Name the blood parasite species.
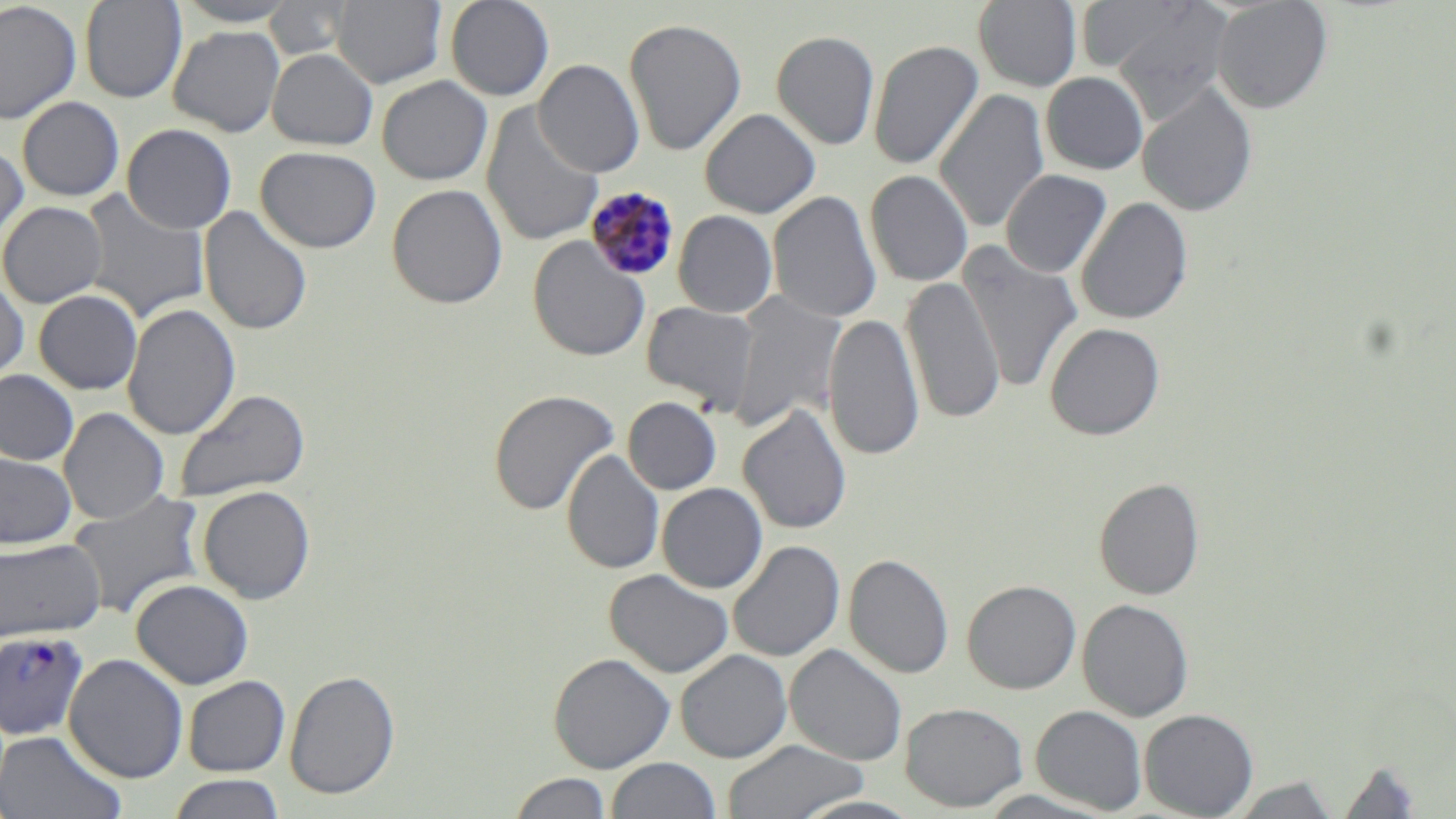

Plasmodium malariae.

Summary:
  - Coordinate format: approximate bounding boxes as named x1/y1/x2/y2 corners in pixels
  - Uninfected red blood cell locations: (x1=79, y1=0, x2=186, y2=102), (x1=172, y1=0, x2=300, y2=27), (x1=266, y1=0, x2=355, y2=62), (x1=332, y1=0, x2=446, y2=87), (x1=445, y1=0, x2=555, y2=101), (x1=1212, y1=0, x2=1332, y2=113), (x1=0, y1=1, x2=81, y2=124), (x1=973, y1=1, x2=1082, y2=91), (x1=1074, y1=2, x2=1201, y2=76), (x1=1107, y1=5, x2=1231, y2=120), (x1=623, y1=18, x2=747, y2=155), (x1=168, y1=26, x2=284, y2=137), (x1=771, y1=30, x2=880, y2=150), (x1=868, y1=39, x2=983, y2=170), (x1=267, y1=48, x2=378, y2=150), (x1=533, y1=59, x2=645, y2=177), (x1=1041, y1=72, x2=1149, y2=174), (x1=376, y1=75, x2=492, y2=185), (x1=1137, y1=83, x2=1258, y2=216), (x1=935, y1=89, x2=1049, y2=233), (x1=17, y1=96, x2=125, y2=201), (x1=481, y1=103, x2=604, y2=247), (x1=700, y1=108, x2=820, y2=218), (x1=122, y1=124, x2=237, y2=234), (x1=0, y1=142, x2=28, y2=250), (x1=256, y1=146, x2=381, y2=253), (x1=1000, y1=169, x2=1112, y2=277), (x1=865, y1=170, x2=973, y2=286), (x1=387, y1=183, x2=507, y2=309), (x1=79, y1=189, x2=210, y2=324), (x1=768, y1=190, x2=882, y2=324), (x1=1076, y1=197, x2=1193, y2=325), (x1=0, y1=201, x2=107, y2=308), (x1=199, y1=205, x2=312, y2=335), (x1=673, y1=210, x2=777, y2=318), (x1=527, y1=235, x2=650, y2=361), (x1=958, y1=243, x2=1083, y2=393), (x1=901, y1=275, x2=1004, y2=425), (x1=0, y1=276, x2=29, y2=388), (x1=33, y1=289, x2=142, y2=394), (x1=730, y1=290, x2=846, y2=433), (x1=641, y1=301, x2=759, y2=412), (x1=122, y1=302, x2=240, y2=439), (x1=824, y1=312, x2=924, y2=463), (x1=1045, y1=321, x2=1165, y2=440), (x1=0, y1=370, x2=79, y2=466), (x1=174, y1=388, x2=310, y2=502), (x1=488, y1=389, x2=619, y2=515), (x1=623, y1=397, x2=721, y2=495), (x1=738, y1=404, x2=853, y2=534), (x1=59, y1=407, x2=169, y2=524), (x1=562, y1=450, x2=665, y2=574), (x1=0, y1=451, x2=77, y2=550), (x1=1094, y1=477, x2=1205, y2=600), (x1=657, y1=482, x2=768, y2=593), (x1=197, y1=485, x2=316, y2=604), (x1=67, y1=490, x2=207, y2=621), (x1=0, y1=538, x2=106, y2=643), (x1=728, y1=540, x2=845, y2=662), (x1=844, y1=553, x2=954, y2=679), (x1=604, y1=569, x2=734, y2=678), (x1=131, y1=579, x2=254, y2=689), (x1=962, y1=579, x2=1081, y2=694), (x1=1077, y1=598, x2=1193, y2=721), (x1=785, y1=644, x2=907, y2=765), (x1=675, y1=649, x2=792, y2=762), (x1=548, y1=652, x2=675, y2=773), (x1=64, y1=653, x2=188, y2=783), (x1=284, y1=670, x2=400, y2=799), (x1=182, y1=675, x2=290, y2=777), (x1=900, y1=702, x2=1028, y2=812), (x1=1031, y1=705, x2=1147, y2=814), (x1=1140, y1=708, x2=1258, y2=818), (x1=0, y1=730, x2=125, y2=819), (x1=722, y1=739, x2=868, y2=818), (x1=606, y1=758, x2=721, y2=818), (x1=1336, y1=759, x2=1424, y2=819), (x1=507, y1=772, x2=613, y2=818), (x1=165, y1=774, x2=287, y2=818), (x1=1227, y1=776, x2=1339, y2=818)
  - Plasmodium malariae-infected red blood cell locations: (x1=584, y1=186, x2=681, y2=281), (x1=0, y1=628, x2=90, y2=742)
  - Image size: 1456×819 pixels
  - Field of view: single
  - Magnification: 1000x
  - Preparation: thin blood smear
  - Modality: light microscopy
  - Stain: May-Grünwald-Giemsa